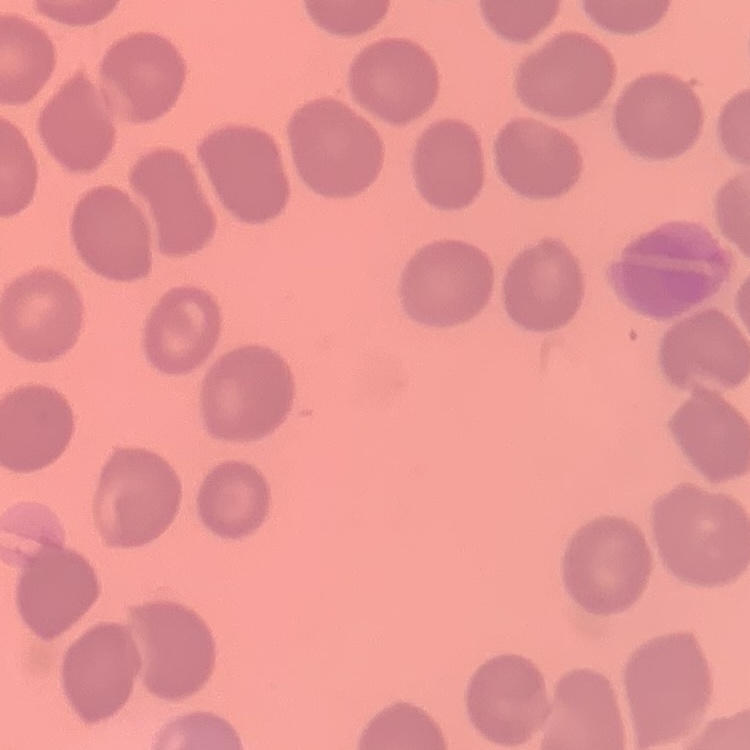

red_blood_cell_morphology: no rouleaux formation
stain: Field's or Giemsa
preparation: thin blood smear
image_type: square crop of a larger photomicrograph